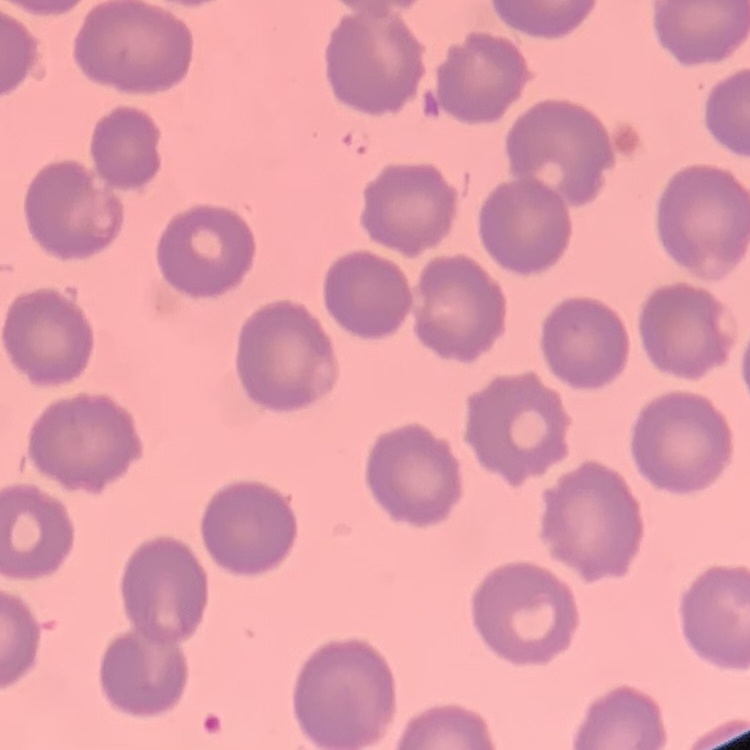
erythrocyte morphology = no rouleaux formation
preparation = thin blood film
image type = square crop of a larger photomicrograph
stain = Field's or Giemsa